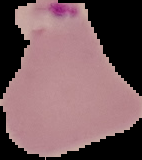
image size = 142×160 pixels
result = malaria parasites detected
preparation = thin blood smear
image type = segmented cell region with the area outside set to black